Locate every blood parasite and identify its species.
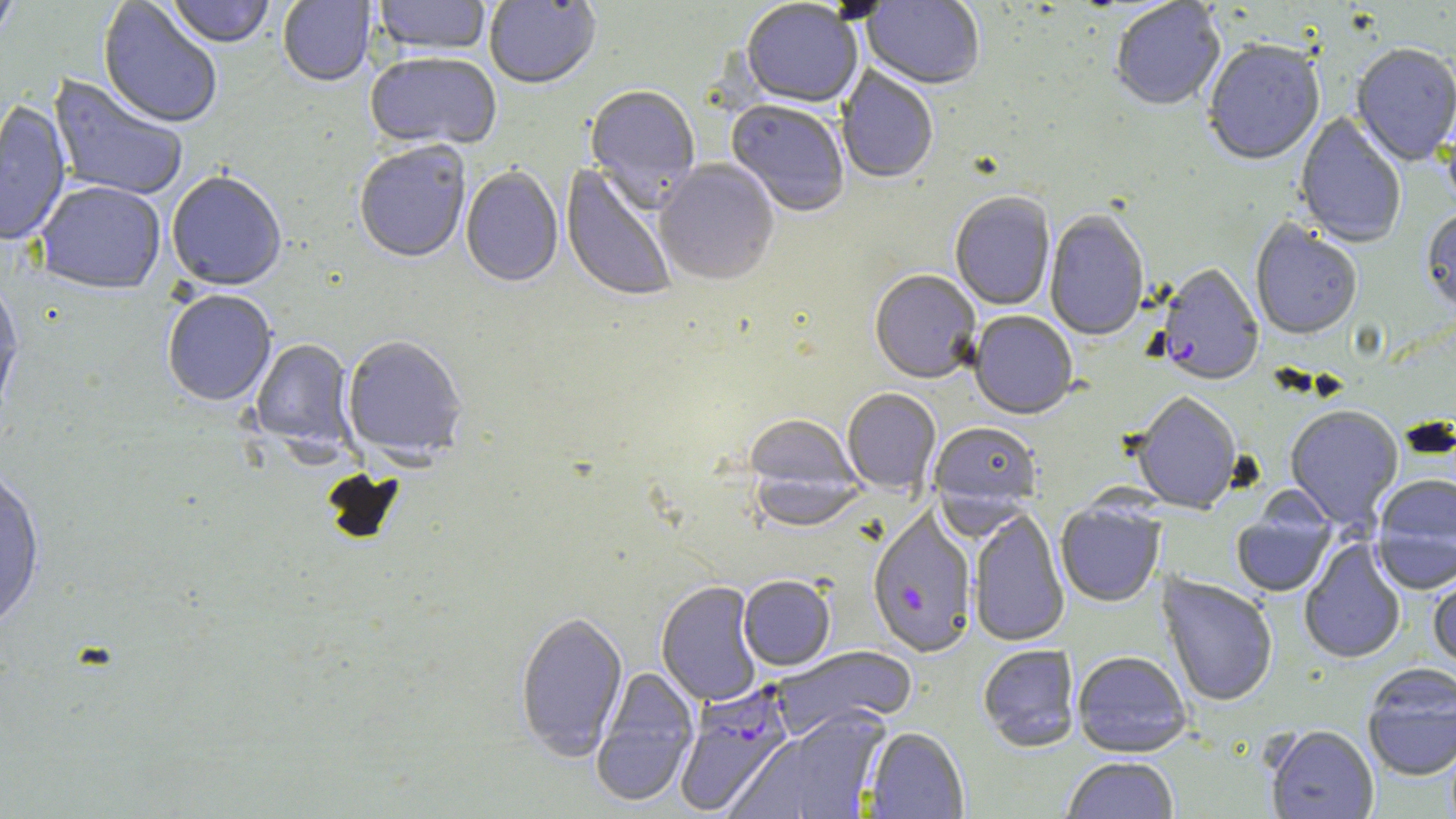
Approximate bounding boxes as (x1, y1, x2, y2) in pixels.
Plasmodium falciparum-infected red blood cells: (1156, 265, 1264, 388), (674, 683, 795, 817).
No Plasmodium ovale, Plasmodium malariae, Plasmodium vivax, Babesia divergens, or Trypanosoma brucei observed.

Uninfected red blood cell locations: (0, 0, 21, 47), (98, 0, 223, 130), (167, 0, 274, 50), (278, 0, 375, 88), (373, 0, 491, 58), (484, 1, 601, 91), (861, 1, 984, 91), (741, 2, 862, 110), (1111, 2, 1225, 112), (1203, 43, 1325, 168), (1351, 45, 1456, 168), (365, 54, 502, 153), (836, 65, 938, 186), (47, 74, 188, 202), (585, 87, 701, 210), (0, 101, 71, 246), (725, 101, 849, 218), (1295, 112, 1406, 250), (354, 144, 471, 265), (654, 160, 780, 288), (560, 163, 679, 304), (460, 167, 563, 289), (166, 172, 287, 292), (33, 181, 166, 296), (950, 193, 1055, 311), (1044, 211, 1149, 343), (1420, 211, 1456, 320), (1250, 221, 1362, 342), (869, 271, 981, 384), (0, 279, 23, 423), (162, 291, 277, 408), (969, 312, 1078, 421), (342, 337, 468, 464), (251, 339, 357, 455), (842, 389, 941, 495), (1131, 394, 1241, 514), (1284, 407, 1403, 531), (743, 416, 861, 528), (929, 422, 1040, 513), (0, 466, 45, 636), (1372, 477, 1456, 593), (1231, 500, 1337, 599), (1056, 501, 1166, 608), (867, 509, 977, 659), (968, 509, 1070, 647), (1299, 538, 1407, 665), (1428, 568, 1456, 674), (1157, 574, 1278, 708), (738, 576, 836, 671), (656, 581, 762, 707), (515, 612, 628, 761), (978, 645, 1080, 753), (770, 646, 917, 739), (1072, 651, 1193, 758), (1362, 666, 1456, 782), (590, 667, 699, 808), (730, 709, 891, 819), (1265, 726, 1379, 819), (864, 727, 969, 818), (1062, 758, 1179, 819). Slide-level diagnosis: Plasmodium falciparum. Thin blood film. 1000x magnification. Optical microscopy. Image is 1456×819 pixels. May-Grünwald-Giemsa stain. One field of a larger specimen.